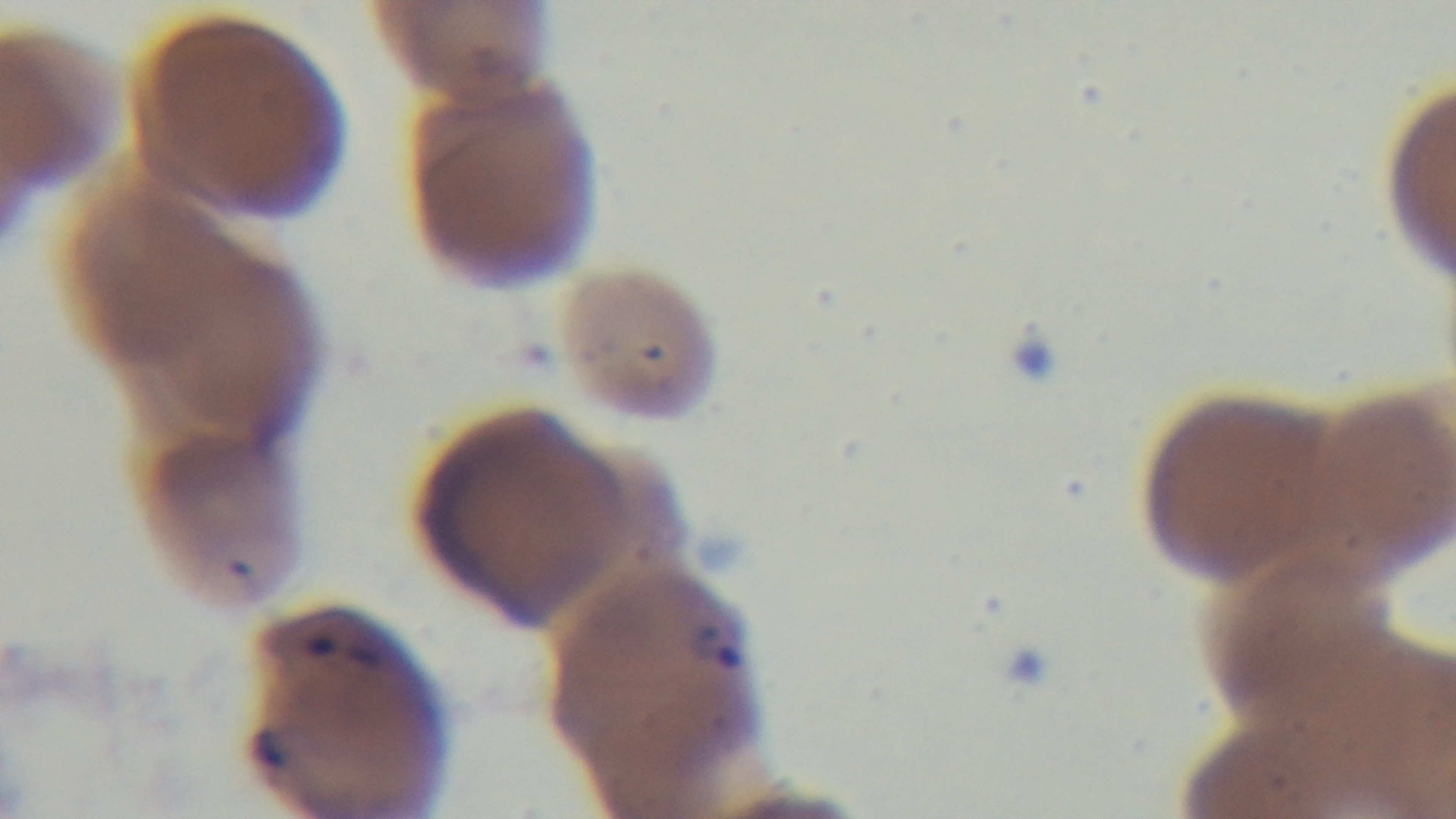

stain: Giemsa
preparation: thin smear
capture: mounted 4K digital camera
objective: 100x oil immersion
malaria_status: infected
field_of_view: single
modality: light microscopy